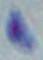
Photomicrograph. Captured at 1000x magnification. Toxoplasma gondii is seen.